Report the malaria status of this cell.
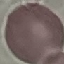
Uninfected.

{
  "stain": "Giemsa",
  "preparation": "thin blood smear",
  "capture": "smartphone camera at the microscope eyepiece",
  "image_type": "automatically extracted cell patch, resized to 64 × 64 pixels"
}